State which parasite is depicted.
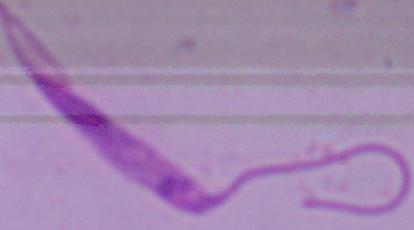

Leishmania.

Summary:
  - Magnification: 1000x
  - Modality: photomicrograph